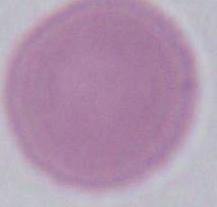

Photomicrograph. Captured at 1000x magnification. A red blood cell is seen.